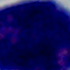
Summary:
  - Modality: micrograph
  - Identification: leukocyte
  - Magnification: 1000x